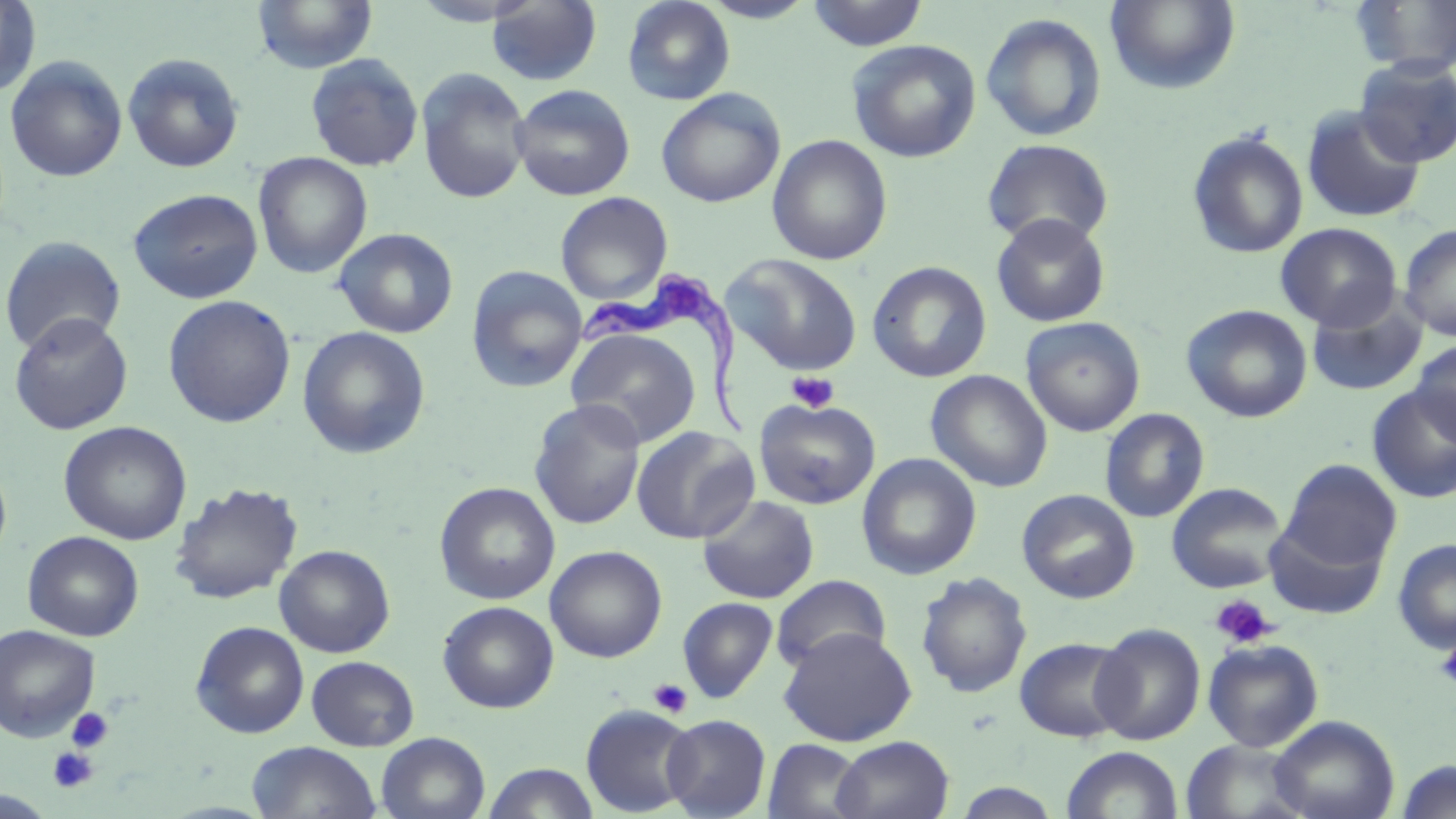

slide-level diagnosis = Trypanosoma brucei
magnification = 1000x
uninfected red blood cell locations = approximate bounding boxes as (x1, y1, x2, y2) in pixels: (622, 0, 735, 105), (1105, 0, 1241, 94), (0, 1, 41, 98), (252, 1, 378, 74), (487, 1, 602, 86), (699, 1, 818, 23), (805, 1, 930, 51), (1352, 1, 1456, 76), (980, 12, 1107, 142), (846, 39, 981, 162), (122, 52, 245, 173), (305, 53, 424, 172), (5, 56, 128, 183), (1353, 57, 1456, 167), (415, 67, 532, 205), (510, 84, 636, 201), (656, 88, 785, 207), (1301, 106, 1426, 223), (1187, 129, 1309, 259), (767, 135, 893, 265), (982, 138, 1114, 249), (252, 152, 373, 279), (128, 188, 264, 304), (555, 191, 673, 305), (990, 213, 1111, 327), (1275, 223, 1401, 331), (1399, 223, 1456, 340), (333, 228, 459, 339), (0, 235, 126, 356), (724, 254, 864, 376), (867, 261, 992, 383), (466, 265, 587, 393), (1306, 291, 1428, 398), (163, 295, 296, 428), (1181, 304, 1313, 423), (8, 312, 133, 435), (1020, 316, 1146, 437), (565, 325, 702, 449), (297, 326, 431, 459), (1411, 340, 1456, 446), (925, 369, 1053, 492), (1366, 385, 1456, 504), (754, 397, 881, 510), (529, 399, 646, 530), (1099, 408, 1210, 523), (58, 421, 192, 545), (631, 427, 759, 544), (0, 453, 12, 572), (857, 453, 981, 580), (1280, 459, 1401, 572), (169, 482, 303, 604), (434, 482, 560, 604), (1166, 482, 1289, 594), (1017, 489, 1140, 603), (697, 495, 819, 604), (1263, 514, 1390, 620), (23, 531, 144, 641), (1392, 538, 1456, 654), (275, 544, 395, 657), (545, 545, 667, 663), (915, 571, 1032, 698), (771, 574, 891, 674), (677, 597, 778, 703), (437, 601, 559, 713), (190, 621, 309, 739), (1, 624, 101, 741), (1091, 624, 1205, 745), (778, 626, 917, 746), (1014, 636, 1133, 743), (1203, 638, 1323, 752), (306, 656, 419, 751), (581, 704, 698, 817), (661, 714, 771, 818), (1268, 715, 1399, 819), (376, 732, 490, 819), (831, 735, 954, 819), (763, 739, 867, 819), (1180, 739, 1311, 819), (247, 742, 382, 819), (1062, 746, 1183, 819), (1395, 760, 1456, 818), (482, 762, 600, 819), (950, 780, 1067, 818), (0, 790, 57, 818)
platelet locations = approximate bounding boxes as (x1, y1, x2, y2) in pixels: (787, 371, 839, 413), (1211, 594, 1276, 650), (1436, 640, 1456, 690), (647, 678, 693, 718), (66, 707, 114, 753), (47, 747, 99, 793)
Trypanosoma brucei locations = approximate bounding boxes as (x1, y1, x2, y2) in pixels: (574, 272, 751, 437)
field of view = single
stain = May-Grünwald-Giemsa
image size = 1456×819 pixels
preparation = thin blood film
modality = light microscopy